Report the malaria status.
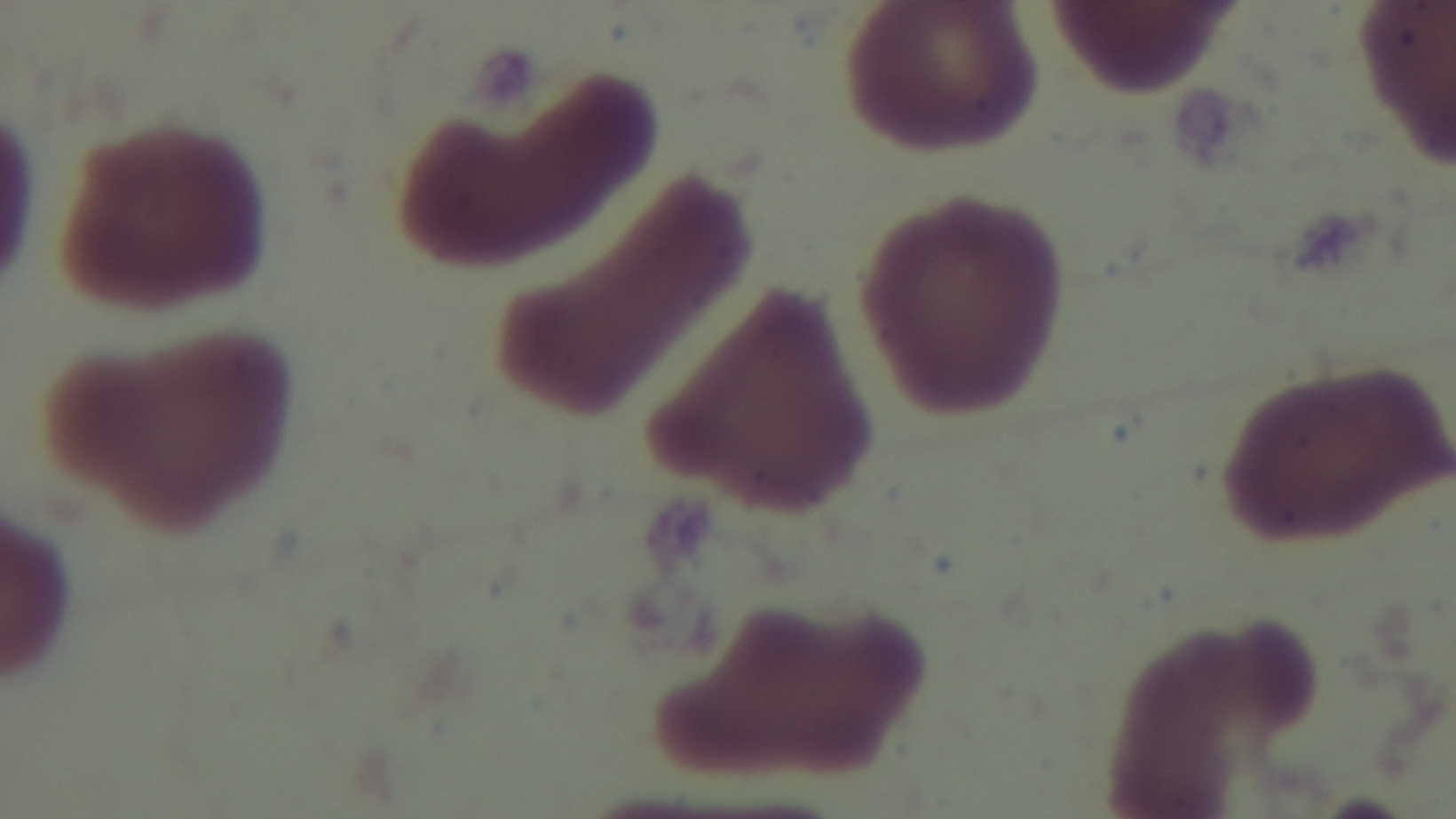

Negative.

preparation = thin smear
capture = mounted 4K digital camera
objective = 100x oil immersion
field of view = single
modality = light microscopy
stain = Giemsa